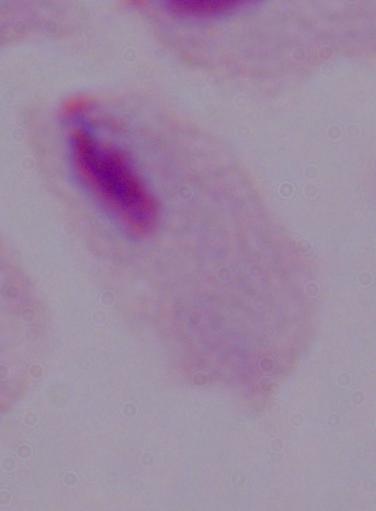
modality = micrograph
magnification = 1000x
identification = trichomonad